Outline each uninfected red blood cell.
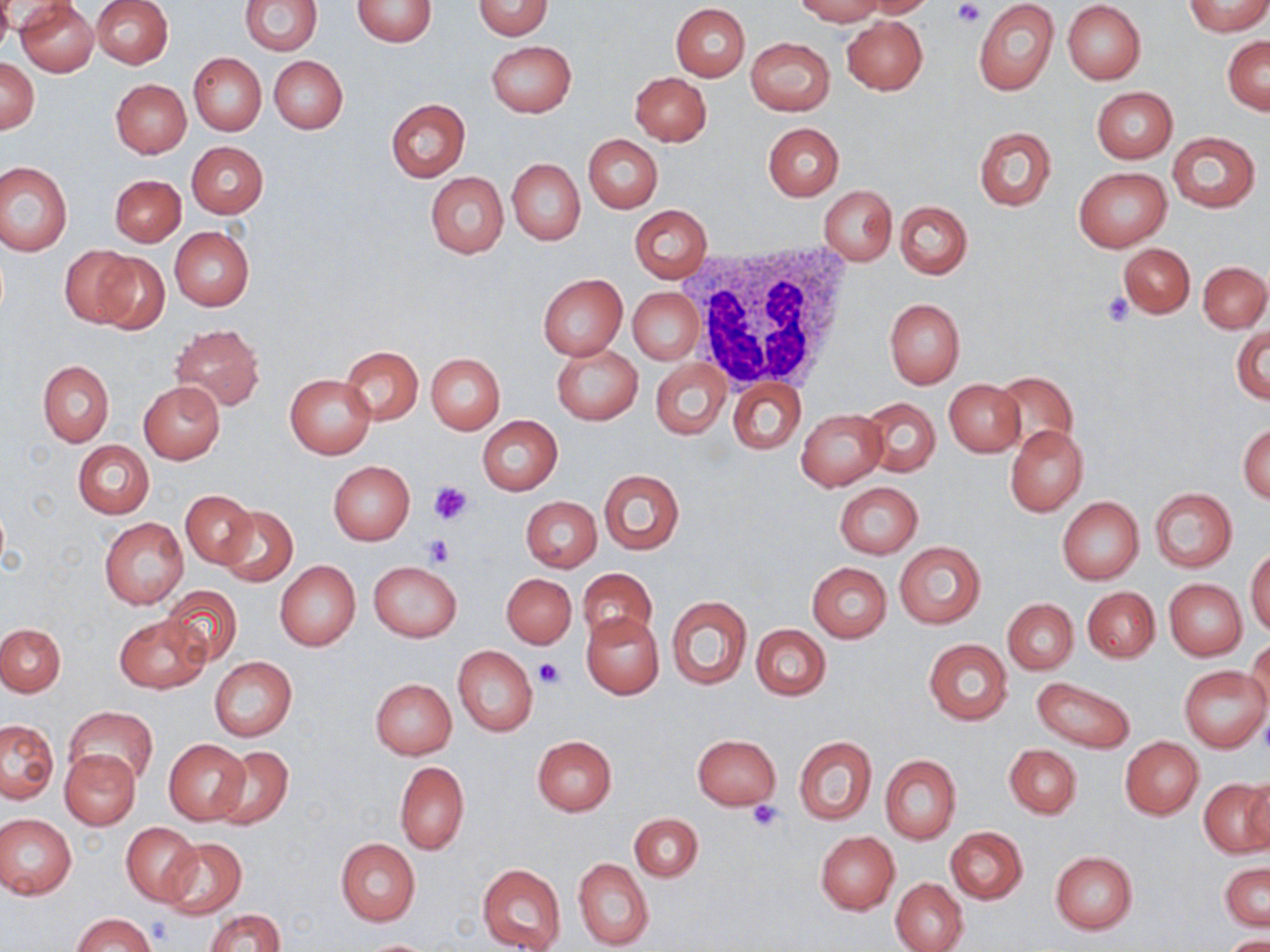

Approximate bounding boxes as (x1,y1)-(x2,y2) corner pairs in pixels.
Uninfected red blood cells: (17,0)-(98,76), (91,0)-(173,68), (240,0)-(321,56), (352,0)-(436,46), (473,0)-(553,39), (794,0)-(885,24), (858,0)-(935,18), (0,1)-(15,52), (1062,1)-(1146,85), (973,2)-(1059,96), (1184,2)-(1270,36), (670,3)-(751,81), (842,16)-(928,95), (1224,36)-(1270,114), (747,37)-(834,115), (486,39)-(576,117), (189,53)-(266,135), (270,56)-(348,133), (0,58)-(40,134), (630,72)-(711,145), (111,79)-(192,157), (1091,86)-(1178,162), (386,98)-(471,181), (763,122)-(844,200), (972,125)-(1056,212), (1167,131)-(1260,212), (584,134)-(663,213), (187,141)-(268,218), (507,158)-(585,245), (0,162)-(73,257), (1074,167)-(1171,252), (425,171)-(509,259), (110,175)-(185,246), (820,185)-(896,265), (894,200)-(972,279), (629,205)-(713,283), (169,226)-(253,311), (1117,242)-(1194,318), (61,247)-(142,327), (91,250)-(170,334), (1199,262)-(1269,332), (538,274)-(628,359), (629,288)-(704,365), (884,298)-(965,388), (169,324)-(266,411), (1232,324)-(1269,405), (553,344)-(642,424), (341,345)-(422,424), (426,353)-(505,434), (652,359)-(731,439), (38,360)-(114,446), (990,370)-(1080,455), (285,374)-(376,458), (729,379)-(805,454), (943,379)-(1025,456), (138,381)-(226,463), (863,397)-(940,478), (797,408)-(889,489), (477,416)-(563,495), (1239,422)-(1269,504), (1005,425)-(1088,515), (73,441)-(154,517), (327,460)-(415,546), (599,469)-(684,554), (835,482)-(923,558), (1149,488)-(1237,572), (181,490)-(257,569), (520,496)-(602,573), (1057,497)-(1144,583), (217,506)-(297,587), (100,518)-(188,609), (894,542)-(985,629), (1247,548)-(1270,635), (274,560)-(360,652), (370,561)-(461,642), (807,562)-(891,643), (577,567)-(657,646), (502,573)-(577,650), (1165,579)-(1247,660), (161,585)-(243,665), (1083,586)-(1160,662), (666,594)-(751,690), (1003,599)-(1078,674), (581,611)-(663,700), (114,614)-(209,694), (0,623)-(66,696), (751,624)-(831,700), (1247,637)-(1270,715), (924,639)-(1012,724), (453,645)-(538,737), (210,659)-(297,740), (1179,666)-(1268,753), (1031,677)-(1136,754), (370,679)-(456,759), (66,706)-(157,787), (0,719)-(58,802), (692,734)-(781,810), (532,735)-(616,815), (795,737)-(876,824), (1120,738)-(1203,819), (164,739)-(251,825), (1005,744)-(1081,819), (211,746)-(294,830), (62,749)-(140,828), (879,754)-(961,845), (395,762)-(469,854), (1244,776)-(1270,855), (1198,779)-(1268,857), (630,813)-(702,882), (1,814)-(76,898), (122,822)-(201,905), (946,827)-(1027,904), (816,832)-(899,913), (160,838)-(246,919), (335,838)-(420,926), (1050,851)-(1138,933), (573,858)-(653,950), (1221,862)-(1269,931), (477,863)-(567,951), (891,878)-(968,952), (206,908)-(285,952), (73,914)-(156,952), (1221,934)-(1270,952), (355,939)-(438,951).

White blood cell locations: (685,244)-(853,389). Platelet locations: (951,0)-(983,26), (1101,291)-(1134,327), (430,481)-(473,524), (425,534)-(456,566), (535,658)-(565,687), (747,800)-(785,832). Slide-level diagnosis: negative for blood parasites. Thin blood film. Captured at 1000x magnification. Image is 1270×952 pixels. Light microscopy. One field of a larger specimen. May-Grünwald-Giemsa-stained preparation.